Assess this cell for malaria.
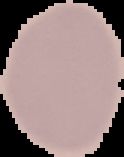

It is uninfected.

Summary:
  - Preparation: thin blood film
  - Image type: cell region segmented out of the field of view; surrounding area masked to black
  - Image size: 124×157 pixels